Classify this cell by malaria status.
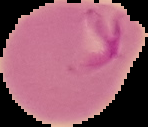

It is parasitized.

Cell region segmented out of the field of view; the surrounding area is masked to black. Image is 148×127 pixels. From a thin blood smear.